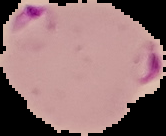

Summary:
  - Image size: 166×136 pixels
  - Result: Plasmodium parasites identified
  - Preparation: thin blood smear
  - Image type: segmented cell region on a black background